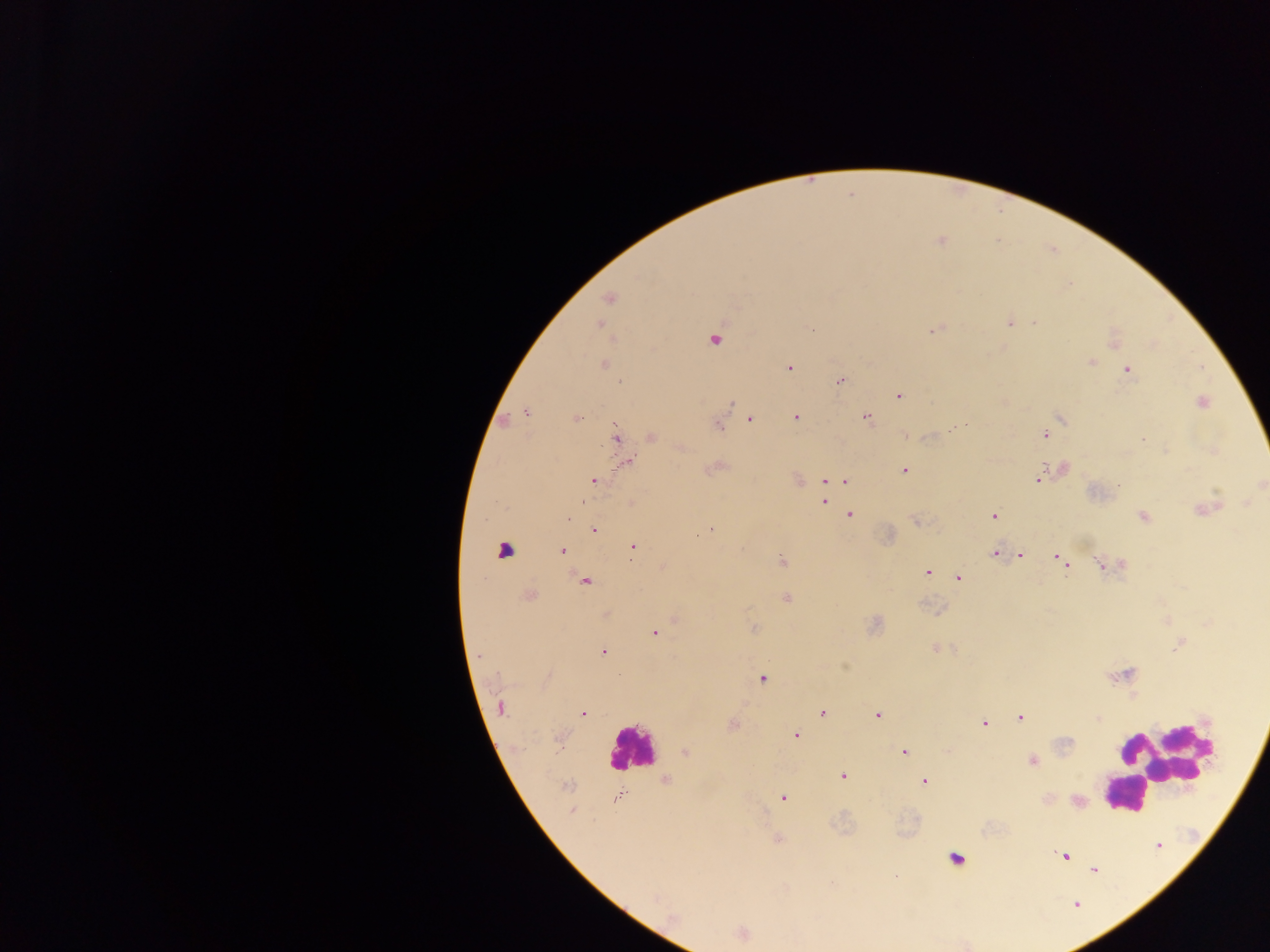
Approximate centers as (x, y) in pixels.
Summary:
  - Plasmodium parasite locations: (941, 242), (608, 299), (1011, 323), (1035, 323), (599, 325), (810, 329), (933, 331), (714, 340), (1091, 362), (605, 365), (1201, 367), (789, 368), (1127, 369), (840, 381), (899, 396), (1202, 403), (730, 406), (526, 412), (865, 417), (575, 418), (795, 418), (1062, 418), (750, 419), (718, 426), (1045, 434), (616, 435), (652, 436), (1143, 439), (627, 462), (903, 470), (841, 480), (1039, 480), (594, 481), (827, 481), (1261, 484), (824, 501), (1207, 508), (849, 515), (994, 516), (1144, 516), (711, 529), (594, 530), (697, 537), (633, 547), (562, 550), (994, 554), (1021, 555), (1062, 561), (782, 562), (1102, 565), (927, 572), (958, 578), (585, 581), (529, 595), (787, 598), (754, 628), (654, 633), (603, 651), (479, 655), (762, 679), (501, 708), (823, 713), (582, 714), (877, 715), (1020, 718), (1099, 718), (984, 723), (733, 725), (796, 736), (685, 752), (903, 752), (1032, 762), (842, 776), (665, 781), (924, 782), (567, 785), (615, 798), (783, 798), (572, 811), (778, 839), (1064, 856), (1094, 870), (742, 935)
  - Leukocyte locations: (506, 550), (631, 748), (1162, 760), (1124, 787), (956, 855)
  - Field of view: single
  - Image size: 1270×952 pixels
  - Country: Ghana
  - Preparation: thick blood smear
  - Capture: mobile-phone photograph through a microscope